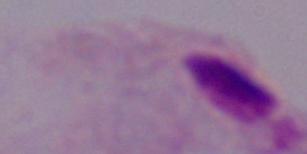
modality = photomicrograph
magnification = 1000x
identification = trichomonad